Give the extent of all Trypanosoma brucei.
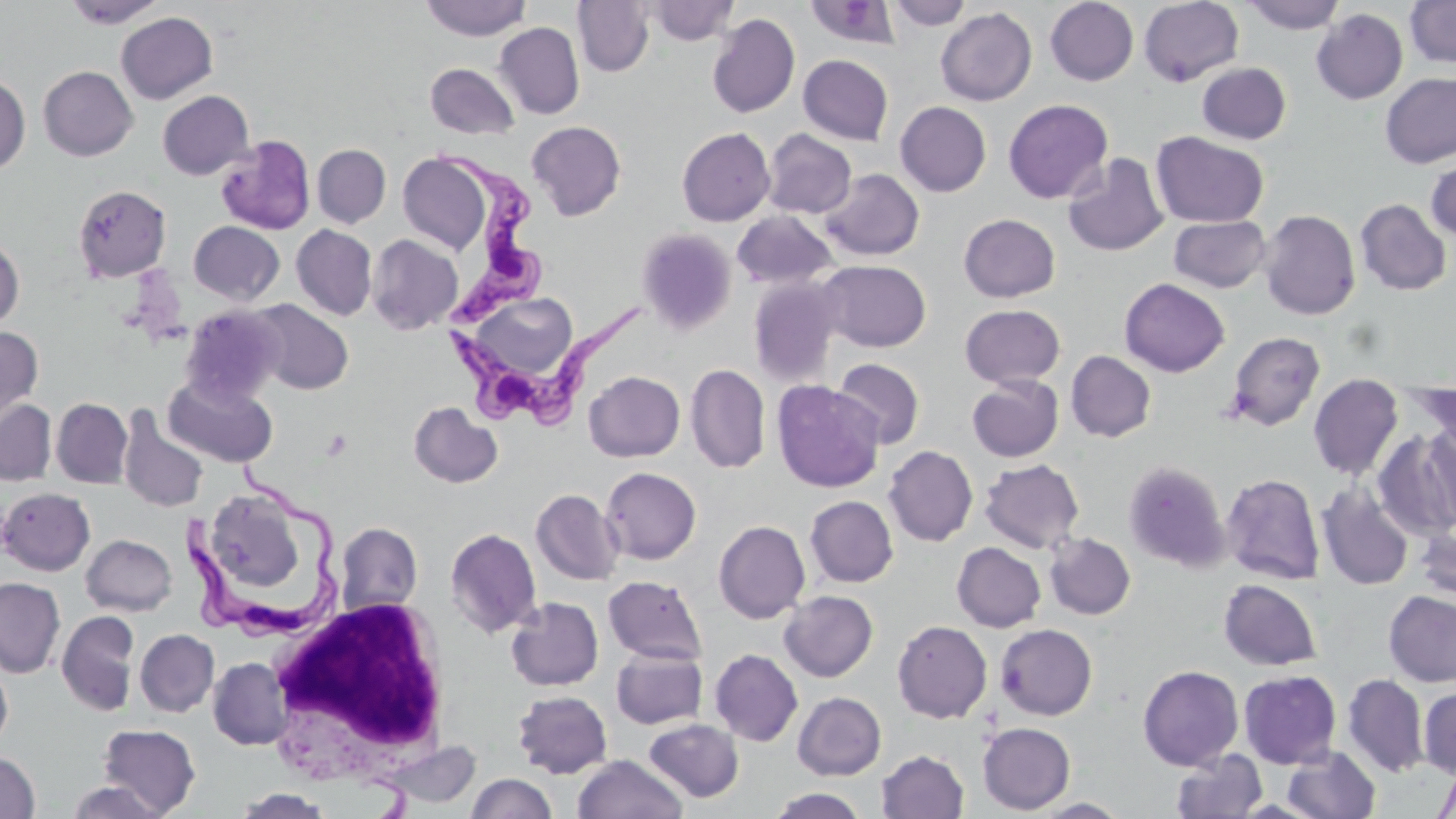

Approximate bounding boxes as named x1/y1/x2/y2 corners in pixels.
Trypanosoma brucei: (x1=434, y1=141, x2=554, y2=330), (x1=444, y1=298, x2=658, y2=423), (x1=180, y1=456, x2=339, y2=644).

White blood cell locations: (x1=266, y1=594, x2=453, y2=785). Uninfected red blood cell locations: (x1=62, y1=0, x2=168, y2=29), (x1=421, y1=0, x2=530, y2=40), (x1=573, y1=0, x2=655, y2=76), (x1=886, y1=0, x2=973, y2=30), (x1=1045, y1=0, x2=1139, y2=85), (x1=1139, y1=0, x2=1243, y2=86), (x1=1241, y1=0, x2=1346, y2=33), (x1=1404, y1=0, x2=1456, y2=68), (x1=644, y1=1, x2=739, y2=45), (x1=806, y1=1, x2=902, y2=48), (x1=935, y1=7, x2=1037, y2=106), (x1=1312, y1=9, x2=1408, y2=104), (x1=116, y1=12, x2=217, y2=104), (x1=707, y1=13, x2=800, y2=118), (x1=495, y1=22, x2=584, y2=119), (x1=798, y1=54, x2=893, y2=145), (x1=1197, y1=62, x2=1291, y2=144), (x1=425, y1=63, x2=520, y2=139), (x1=38, y1=66, x2=138, y2=161), (x1=1380, y1=72, x2=1455, y2=169), (x1=0, y1=74, x2=30, y2=174), (x1=157, y1=90, x2=254, y2=180), (x1=1003, y1=99, x2=1113, y2=204), (x1=895, y1=101, x2=991, y2=197), (x1=527, y1=121, x2=627, y2=221), (x1=677, y1=127, x2=775, y2=226), (x1=762, y1=129, x2=857, y2=218), (x1=1151, y1=131, x2=1269, y2=227), (x1=216, y1=135, x2=316, y2=235), (x1=313, y1=144, x2=391, y2=228), (x1=398, y1=152, x2=493, y2=254), (x1=1062, y1=152, x2=1169, y2=256), (x1=1425, y1=155, x2=1456, y2=243), (x1=820, y1=169, x2=925, y2=261), (x1=72, y1=184, x2=171, y2=282), (x1=1355, y1=199, x2=1452, y2=295), (x1=1259, y1=209, x2=1361, y2=320), (x1=731, y1=210, x2=839, y2=289), (x1=959, y1=213, x2=1060, y2=302), (x1=1169, y1=215, x2=1271, y2=292), (x1=189, y1=220, x2=285, y2=305), (x1=291, y1=224, x2=378, y2=320), (x1=636, y1=228, x2=736, y2=334), (x1=0, y1=234, x2=24, y2=331), (x1=366, y1=234, x2=463, y2=334), (x1=817, y1=260, x2=931, y2=352), (x1=748, y1=277, x2=845, y2=386), (x1=1119, y1=278, x2=1230, y2=376), (x1=461, y1=293, x2=583, y2=385), (x1=248, y1=300, x2=353, y2=394), (x1=960, y1=304, x2=1065, y2=388), (x1=180, y1=305, x2=286, y2=405), (x1=0, y1=325, x2=43, y2=423), (x1=1226, y1=331, x2=1325, y2=431), (x1=1065, y1=351, x2=1156, y2=442), (x1=832, y1=358, x2=925, y2=449), (x1=685, y1=364, x2=770, y2=474), (x1=584, y1=371, x2=685, y2=461), (x1=1308, y1=373, x2=1404, y2=480), (x1=163, y1=374, x2=278, y2=467), (x1=967, y1=375, x2=1063, y2=462), (x1=771, y1=380, x2=885, y2=493), (x1=1409, y1=382, x2=1455, y2=456), (x1=51, y1=398, x2=133, y2=488), (x1=0, y1=399, x2=56, y2=486), (x1=408, y1=401, x2=503, y2=488), (x1=117, y1=406, x2=209, y2=513), (x1=1422, y1=420, x2=1456, y2=530), (x1=1373, y1=430, x2=1456, y2=540), (x1=884, y1=445, x2=978, y2=546), (x1=979, y1=459, x2=1085, y2=554), (x1=1123, y1=460, x2=1231, y2=573), (x1=601, y1=467, x2=701, y2=565), (x1=1221, y1=473, x2=1325, y2=585), (x1=1316, y1=483, x2=1414, y2=591), (x1=0, y1=487, x2=95, y2=575), (x1=531, y1=489, x2=624, y2=586), (x1=209, y1=493, x2=308, y2=591), (x1=805, y1=496, x2=898, y2=587), (x1=713, y1=520, x2=810, y2=623), (x1=335, y1=522, x2=423, y2=616), (x1=1415, y1=524, x2=1456, y2=602), (x1=445, y1=527, x2=541, y2=639), (x1=1045, y1=533, x2=1136, y2=619), (x1=81, y1=534, x2=177, y2=616), (x1=951, y1=542, x2=1046, y2=632), (x1=603, y1=575, x2=708, y2=664), (x1=0, y1=577, x2=65, y2=677), (x1=1219, y1=579, x2=1321, y2=670), (x1=779, y1=590, x2=878, y2=682), (x1=1383, y1=591, x2=1456, y2=686), (x1=506, y1=596, x2=604, y2=690), (x1=56, y1=610, x2=140, y2=716), (x1=893, y1=620, x2=992, y2=723), (x1=995, y1=624, x2=1097, y2=720), (x1=135, y1=629, x2=219, y2=717), (x1=611, y1=648, x2=708, y2=729), (x1=710, y1=648, x2=803, y2=746), (x1=208, y1=657, x2=293, y2=750), (x1=0, y1=661, x2=13, y2=750), (x1=1137, y1=665, x2=1244, y2=770), (x1=1238, y1=670, x2=1342, y2=768), (x1=1342, y1=674, x2=1429, y2=777), (x1=1419, y1=688, x2=1456, y2=777), (x1=512, y1=689, x2=612, y2=778), (x1=792, y1=692, x2=886, y2=780), (x1=644, y1=718, x2=743, y2=802), (x1=978, y1=722, x2=1076, y2=814), (x1=98, y1=724, x2=201, y2=815), (x1=378, y1=740, x2=481, y2=810), (x1=1283, y1=745, x2=1382, y2=819), (x1=1171, y1=749, x2=1268, y2=819), (x1=877, y1=750, x2=968, y2=818), (x1=0, y1=752, x2=40, y2=818), (x1=573, y1=754, x2=688, y2=819), (x1=1434, y1=763, x2=1456, y2=819), (x1=465, y1=773, x2=557, y2=819), (x1=65, y1=780, x2=170, y2=819), (x1=766, y1=788, x2=870, y2=819), (x1=233, y1=789, x2=336, y2=818), (x1=1032, y1=797, x2=1132, y2=817). Slide-level diagnosis: Trypanosoma brucei. Image is 1456×819 pixels. Thin blood smear. One field of a larger specimen. Light microscopy. May-Grünwald-Giemsa-stained preparation. Captured at 1000x magnification.